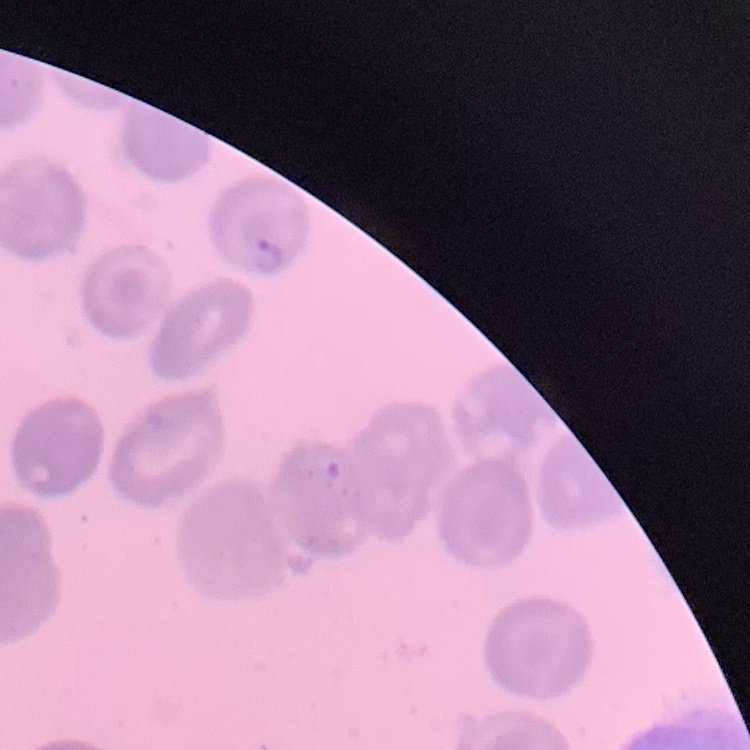

The erythrocytes show no rouleaux formation. Thin blood film. Square crop of a larger photomicrograph. Field's or Giemsa stain.